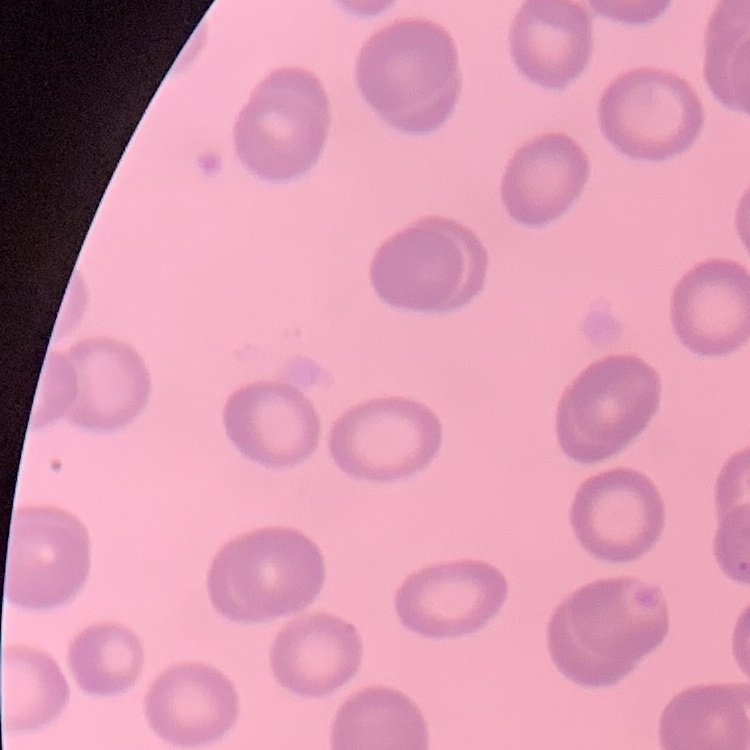

The red blood cells exhibit no rouleaux formation. Stained with either Field's or Giemsa. Thin blood smear. Square crop of a larger photomicrograph.